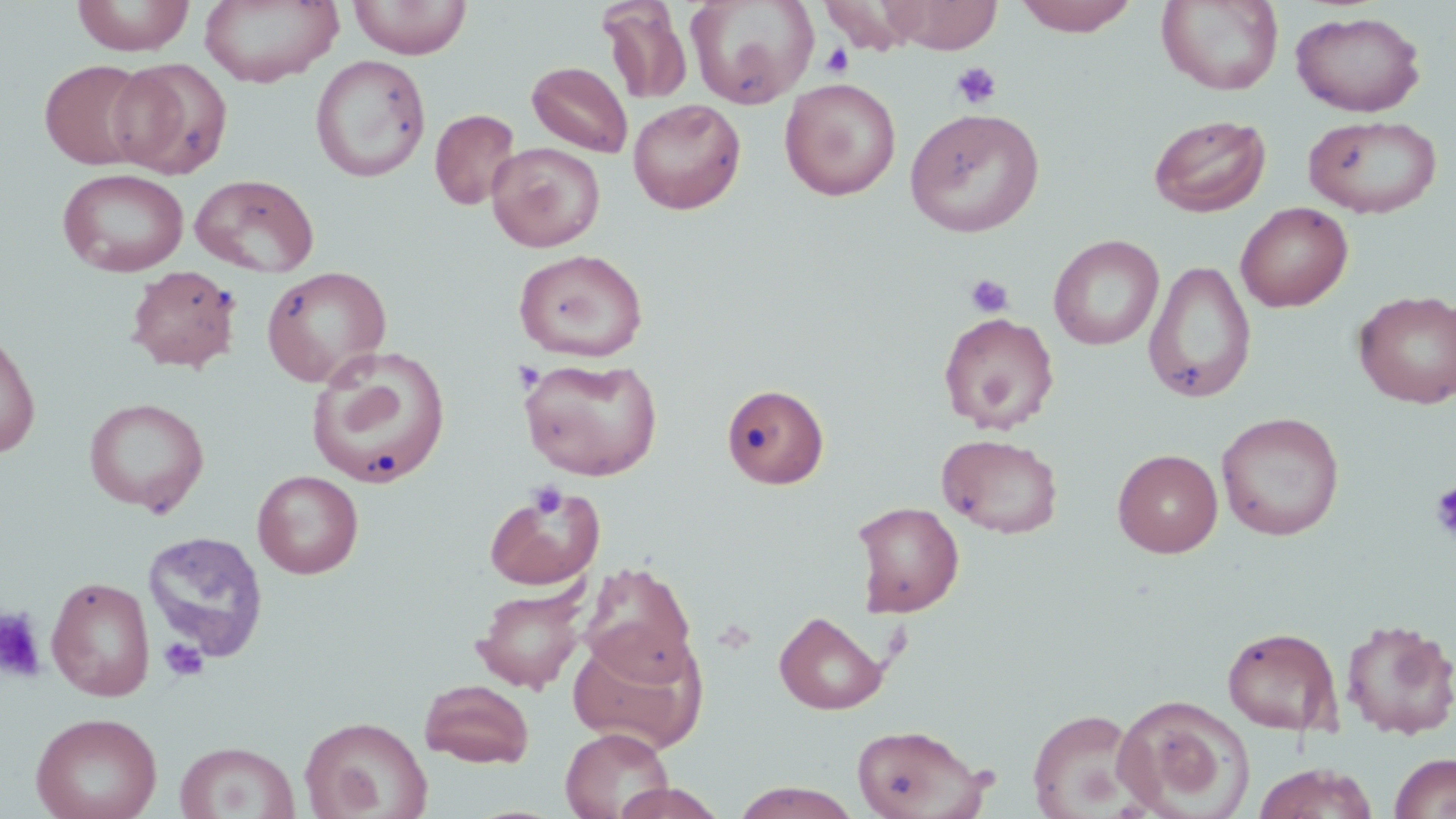
slide-level diagnosis = negative for blood parasites
preparation = thin blood film
image size = 1456×819 pixels
stain = May-Grünwald-Giemsa
magnification = 1000x
uninfected red blood cell locations = approximate bounding boxes as (x1,y1)-(x2,y2) corner pairs in pixels: (72,0)-(195,56), (199,0)-(343,87), (348,0)-(473,59), (685,0)-(819,109), (880,0)-(1002,53), (1013,0)-(1140,36), (1156,1)-(1283,95), (599,3)-(693,103), (1291,11)-(1426,117), (310,54)-(431,183), (110,58)-(232,179), (40,59)-(153,170), (526,61)-(633,157), (780,77)-(902,201), (628,99)-(746,214), (905,107)-(1045,237), (430,109)-(521,210), (1148,113)-(1272,218), (1303,114)-(1443,219), (487,142)-(605,252), (57,167)-(189,277), (190,173)-(319,277), (1235,201)-(1354,312), (1048,234)-(1164,350), (514,248)-(649,362), (1144,259)-(1257,404), (126,265)-(241,373), (261,266)-(392,388), (1354,289)-(1456,409), (938,311)-(1059,432), (0,329)-(41,460), (306,346)-(452,489), (517,356)-(663,481), (721,384)-(829,489), (84,397)-(209,516), (1216,411)-(1345,541), (937,433)-(1062,538), (1113,448)-(1223,558), (252,470)-(363,579), (484,484)-(607,590), (851,501)-(965,617), (142,530)-(268,662), (579,562)-(696,680), (46,575)-(155,702), (473,585)-(588,693), (774,611)-(887,714), (1340,618)-(1456,740), (1222,626)-(1342,735), (567,630)-(708,754), (420,679)-(534,767), (1114,694)-(1255,819), (1027,707)-(1147,818), (30,711)-(162,819), (299,715)-(432,819), (852,723)-(988,819), (561,727)-(673,819), (175,741)-(300,819), (1388,752)-(1456,819), (1252,763)-(1380,819), (728,781)-(866,818), (609,782)-(728,819)
modality = light microscopy
field of view = one of a larger specimen
platelet locations = approximate bounding boxes as (x1,y1)-(x2,y2) corner pairs in pixels: (820,43)-(854,78), (950,61)-(1002,110), (965,273)-(1014,317), (528,480)-(568,520), (1429,481)-(1456,542), (0,608)-(47,683), (158,637)-(208,682)